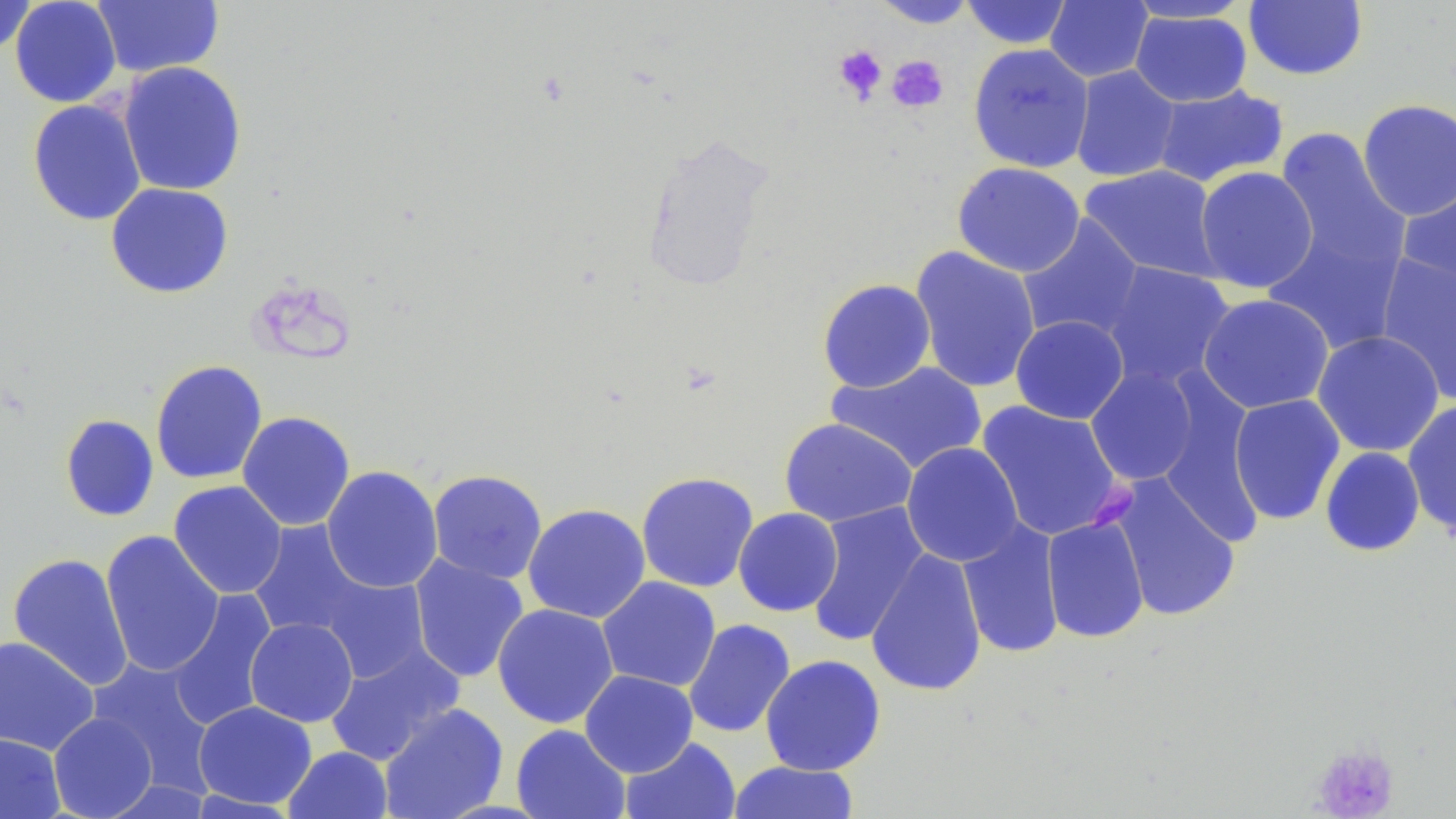
Approximate bounding boxes as named x1/y1/x2/y2 corners in pixels. Platelet locations: (x1=833, y1=45, x2=887, y2=103), (x1=886, y1=55, x2=949, y2=113), (x1=1310, y1=742, x2=1400, y2=818). Uninfected red blood cell locations: (x1=10, y1=0, x2=122, y2=108), (x1=92, y1=0, x2=225, y2=78), (x1=871, y1=0, x2=981, y2=28), (x1=960, y1=0, x2=1074, y2=49), (x1=1120, y1=0, x2=1257, y2=24), (x1=1, y1=1, x2=37, y2=56), (x1=1045, y1=1, x2=1153, y2=83), (x1=1243, y1=1, x2=1368, y2=81), (x1=1129, y1=8, x2=1252, y2=107), (x1=968, y1=43, x2=1094, y2=173), (x1=117, y1=61, x2=248, y2=196), (x1=1070, y1=65, x2=1182, y2=183), (x1=1150, y1=85, x2=1289, y2=188), (x1=27, y1=99, x2=147, y2=226), (x1=1356, y1=99, x2=1456, y2=221), (x1=1273, y1=126, x2=1409, y2=282), (x1=952, y1=162, x2=1086, y2=278), (x1=1080, y1=164, x2=1224, y2=282), (x1=1194, y1=166, x2=1319, y2=293), (x1=1398, y1=176, x2=1456, y2=299), (x1=106, y1=183, x2=234, y2=298), (x1=1017, y1=215, x2=1145, y2=343), (x1=1264, y1=215, x2=1407, y2=357), (x1=910, y1=245, x2=1041, y2=394), (x1=1375, y1=253, x2=1456, y2=404), (x1=1101, y1=262, x2=1236, y2=389), (x1=817, y1=278, x2=936, y2=393), (x1=1197, y1=293, x2=1335, y2=414), (x1=1010, y1=315, x2=1129, y2=424), (x1=1312, y1=330, x2=1445, y2=457), (x1=150, y1=359, x2=268, y2=484), (x1=827, y1=360, x2=988, y2=475), (x1=1085, y1=367, x2=1199, y2=485), (x1=1228, y1=393, x2=1345, y2=526), (x1=976, y1=400, x2=1126, y2=542), (x1=1402, y1=400, x2=1456, y2=538), (x1=237, y1=411, x2=356, y2=531), (x1=59, y1=414, x2=159, y2=522), (x1=779, y1=418, x2=917, y2=527), (x1=901, y1=442, x2=1023, y2=567), (x1=1320, y1=446, x2=1425, y2=557), (x1=321, y1=465, x2=443, y2=593), (x1=428, y1=469, x2=548, y2=584), (x1=635, y1=471, x2=759, y2=593), (x1=1105, y1=473, x2=1241, y2=623), (x1=168, y1=481, x2=287, y2=599), (x1=522, y1=503, x2=651, y2=624), (x1=805, y1=503, x2=930, y2=647), (x1=733, y1=508, x2=843, y2=617), (x1=1042, y1=515, x2=1150, y2=643), (x1=956, y1=518, x2=1065, y2=660), (x1=247, y1=520, x2=375, y2=643), (x1=100, y1=530, x2=224, y2=678), (x1=865, y1=548, x2=988, y2=697), (x1=8, y1=552, x2=134, y2=691), (x1=408, y1=555, x2=529, y2=683), (x1=311, y1=570, x2=432, y2=683), (x1=597, y1=576, x2=721, y2=692), (x1=165, y1=589, x2=278, y2=731), (x1=492, y1=603, x2=619, y2=728), (x1=244, y1=617, x2=358, y2=727), (x1=683, y1=618, x2=796, y2=738), (x1=0, y1=635, x2=99, y2=755), (x1=325, y1=643, x2=464, y2=766), (x1=760, y1=654, x2=887, y2=776), (x1=86, y1=658, x2=217, y2=790), (x1=579, y1=670, x2=698, y2=777), (x1=193, y1=701, x2=317, y2=810), (x1=379, y1=703, x2=508, y2=819), (x1=48, y1=712, x2=158, y2=818), (x1=511, y1=724, x2=631, y2=819), (x1=0, y1=732, x2=65, y2=818), (x1=619, y1=736, x2=741, y2=819), (x1=283, y1=746, x2=393, y2=819), (x1=727, y1=760, x2=861, y2=819). Slide-level diagnosis: negative for blood parasites. Single field of view. Thin blood smear. May-Grünwald-Giemsa-stained preparation. Image is 1456×819 pixels. Captured at 1000x magnification. Optical microscopy.